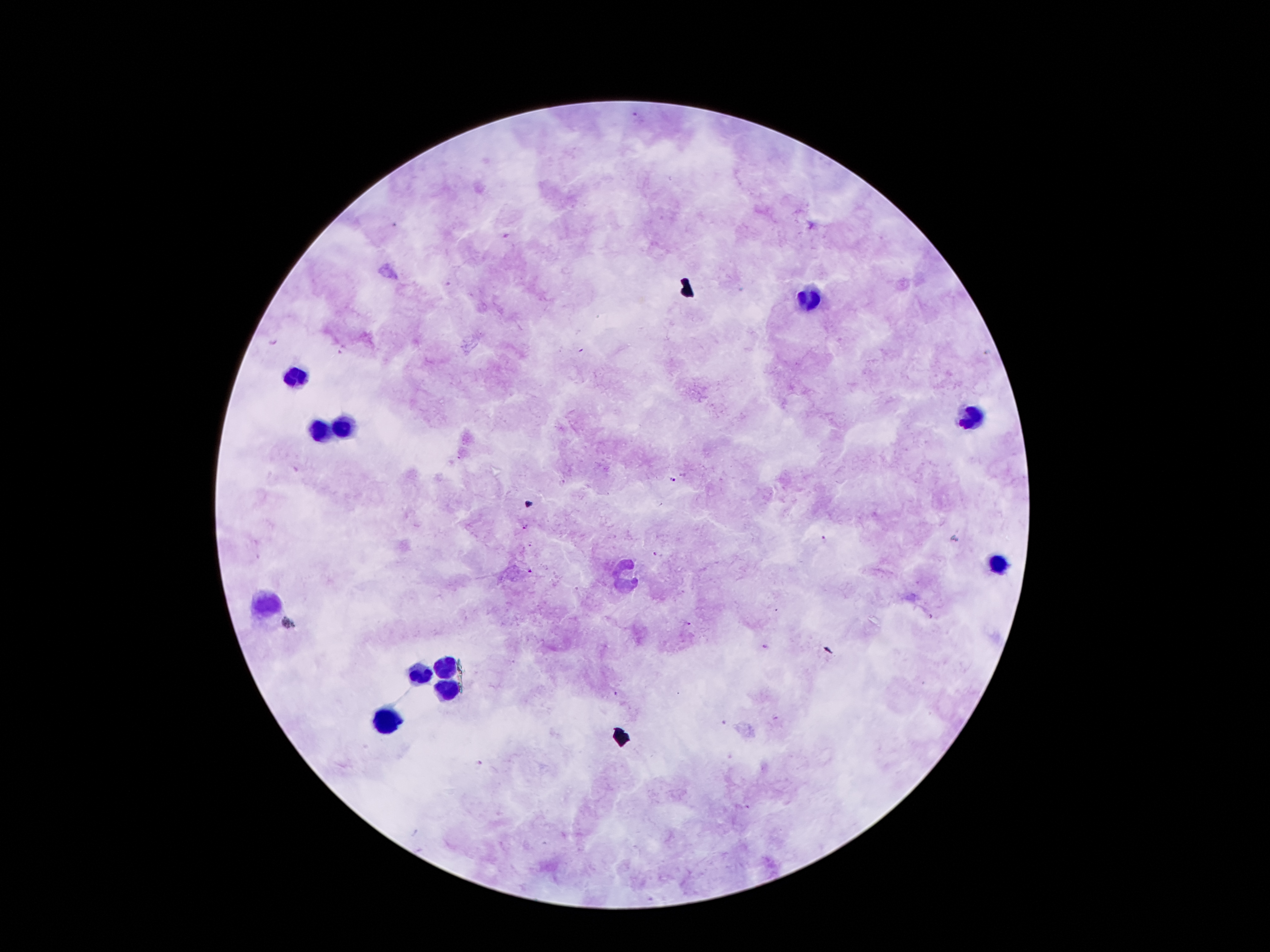 Approximate object centers, in pixels from the top-left corner. Malaria parasite locations: (x=637, y=115), (x=395, y=226), (x=505, y=237), (x=272, y=343), (x=344, y=350), (x=672, y=481), (x=561, y=482), (x=525, y=527), (x=824, y=539), (x=655, y=555), (x=529, y=571), (x=687, y=623), (x=764, y=646). Leukocyte locations: (x=807, y=297), (x=296, y=374), (x=966, y=415), (x=345, y=427), (x=320, y=429), (x=996, y=562), (x=627, y=576), (x=264, y=602), (x=446, y=667), (x=420, y=674), (x=446, y=691), (x=389, y=717). Giemsa stain. 100x magnification. One field from this slide. Image is 1270×952 pixels. Patient malaria status: positive for Plasmodium falciparum. Smartphone photograph taken through the microscope eyepiece. Thick peripheral-blood smear.